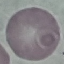
Summary:
  - Result: no malaria parasites seen
  - Stain: Giemsa
  - Preparation: thin smear
  - Image type: cell patch, automatically extracted from a larger field of view and resized to 64 × 64 pixels
  - Capture: smartphone through the microscope eyepiece